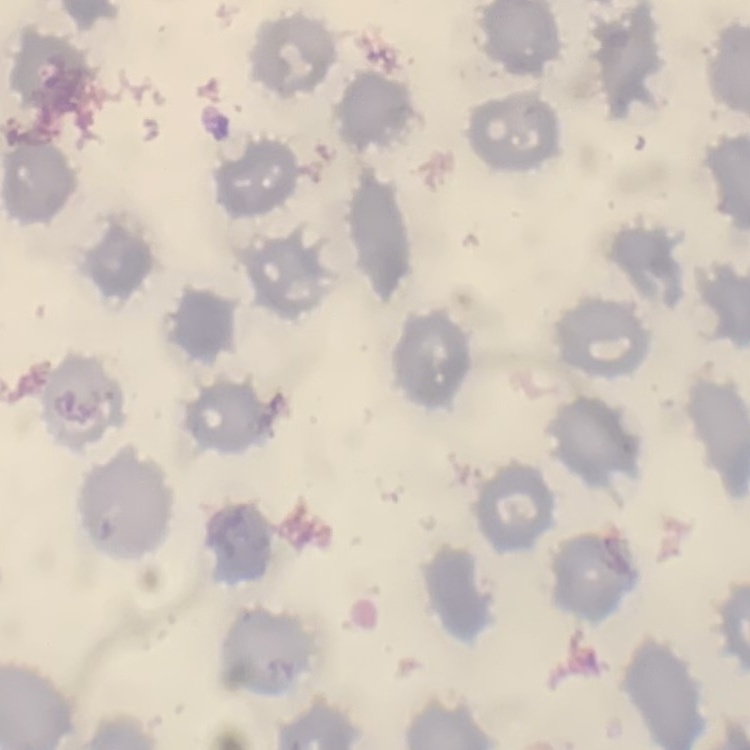
{
  "red_blood_cell_morphology": "no rouleaux formation",
  "image_type": "square crop of a larger photomicrograph",
  "preparation": "thin blood smear",
  "stain": "Field's or Giemsa"
}